Locate every malaria parasite and every leukocyte.
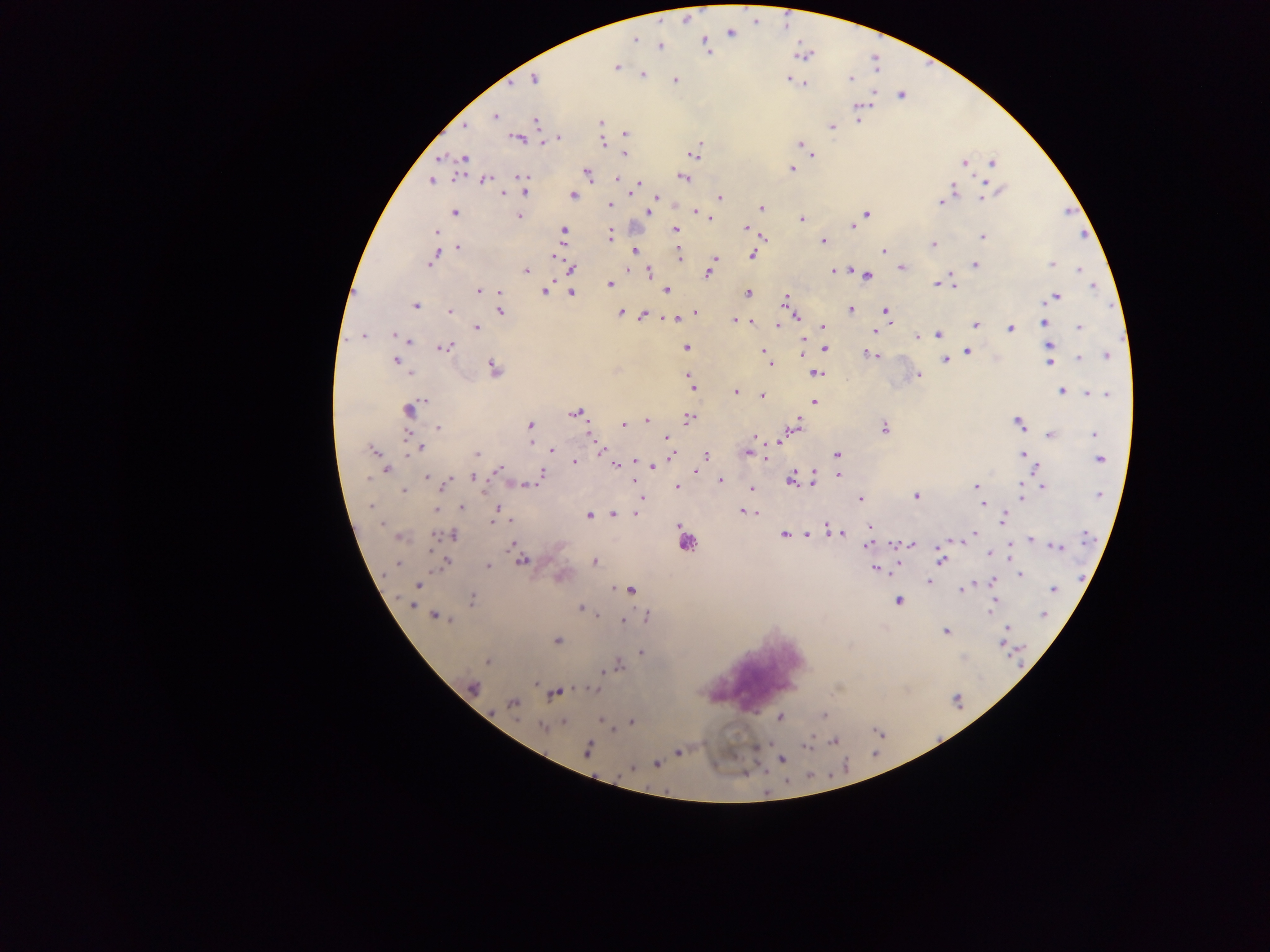
Approximate centers as (x, y) in pixels.
Malaria parasites: (730, 33), (634, 39), (704, 41), (661, 45), (706, 46), (616, 66), (641, 74), (851, 78), (534, 79), (675, 79), (789, 79), (804, 83), (871, 93), (901, 94), (858, 105), (494, 116), (600, 122), (858, 122), (536, 123), (464, 125), (831, 126), (624, 132), (558, 137), (517, 139), (602, 141), (543, 142), (799, 144), (622, 153), (693, 154), (812, 155), (442, 157), (463, 159), (964, 162), (992, 162), (790, 168), (586, 173), (683, 177), (521, 178), (616, 179), (431, 180), (485, 180), (524, 183), (985, 183), (636, 184), (953, 190), (525, 191), (998, 191), (504, 193), (631, 193), (573, 195), (655, 197), (719, 197), (981, 198), (939, 202), (609, 204), (760, 209), (648, 211), (694, 211), (454, 213), (866, 213), (518, 216), (709, 216), (801, 219), (852, 226), (745, 228), (675, 229), (436, 232), (563, 232), (981, 236), (609, 237), (761, 238), (822, 241), (933, 244), (458, 248), (435, 250), (634, 250), (883, 250), (677, 253), (751, 254), (553, 255), (432, 258), (714, 259), (973, 264), (1051, 264), (627, 266), (901, 267), (571, 268), (1079, 269), (525, 271), (833, 271), (649, 272), (708, 272), (867, 275), (949, 281), (938, 283), (610, 284), (953, 286), (1092, 286), (545, 289), (666, 289), (479, 291), (570, 292), (747, 293), (1054, 297), (785, 301), (415, 305), (850, 309), (498, 311), (449, 312), (620, 312), (886, 312), (695, 314), (643, 316), (686, 317), (795, 317), (666, 318), (676, 318), (735, 320), (750, 322), (1043, 322), (778, 325), (975, 325), (476, 327), (823, 327), (1079, 328), (1010, 329), (875, 330), (938, 334), (393, 335), (362, 336), (916, 336), (408, 342), (443, 347), (686, 347), (1050, 347), (824, 349), (967, 352), (766, 353), (803, 354), (869, 354), (1106, 355), (1078, 358), (394, 361), (945, 361), (1050, 361), (768, 362), (493, 368), (815, 372), (410, 374), (688, 374), (918, 374), (689, 382), (691, 387), (734, 391), (1061, 391), (1085, 392), (1107, 394), (762, 395), (813, 401), (409, 408), (575, 413), (688, 417), (646, 420), (623, 423), (1019, 423), (797, 424), (530, 425), (438, 428), (883, 428), (1049, 434), (1094, 434), (592, 435), (666, 437), (753, 438), (781, 440), (529, 442), (420, 448), (598, 448), (373, 450), (552, 450), (603, 451), (746, 452), (476, 454), (1022, 454), (672, 455), (837, 455), (705, 457), (765, 457), (1100, 459), (574, 462), (615, 465), (652, 465), (386, 469), (1036, 470), (500, 471), (695, 472), (541, 473), (837, 475), (426, 477), (473, 478), (813, 478), (634, 479), (791, 480), (444, 481), (719, 481), (523, 484), (975, 486), (1043, 486), (677, 487), (751, 489), (403, 490), (1100, 495), (916, 496), (1021, 496), (640, 499), (859, 499), (981, 502), (370, 505), (461, 506), (437, 508), (496, 510), (742, 511), (757, 513), (613, 514), (634, 514), (588, 515), (496, 519), (1003, 520), (828, 524), (679, 526), (869, 528), (782, 533), (841, 533), (454, 534), (972, 534), (440, 535), (451, 535), (806, 535), (399, 536), (1030, 539), (511, 542), (686, 542), (946, 542), (892, 543), (867, 545), (911, 545), (1056, 546), (987, 552), (1011, 556), (520, 559), (941, 559), (445, 561), (594, 561), (398, 564), (486, 566), (898, 567), (875, 569), (1020, 575), (560, 577), (927, 581), (992, 582), (416, 585), (962, 589), (1053, 589), (630, 590), (995, 599), (898, 600), (471, 601), (582, 608), (990, 613), (599, 614), (1044, 615), (435, 616), (647, 618), (622, 621), (946, 631), (1005, 631), (557, 640), (1001, 643), (640, 652), (488, 661), (616, 666), (600, 671), (535, 684), (472, 688), (595, 688), (552, 694), (513, 703), (823, 716), (780, 717), (601, 720), (563, 721), (631, 722), (542, 728), (834, 740), (808, 746), (587, 750), (677, 752), (782, 759), (656, 763).
Leukocytes: (754, 670).

Summary:
  - Country: Ghana
  - Image size: 1270×952 pixels
  - Preparation: thick blood film
  - Capture: mobile-phone photograph through a microscope
  - Field of view: single